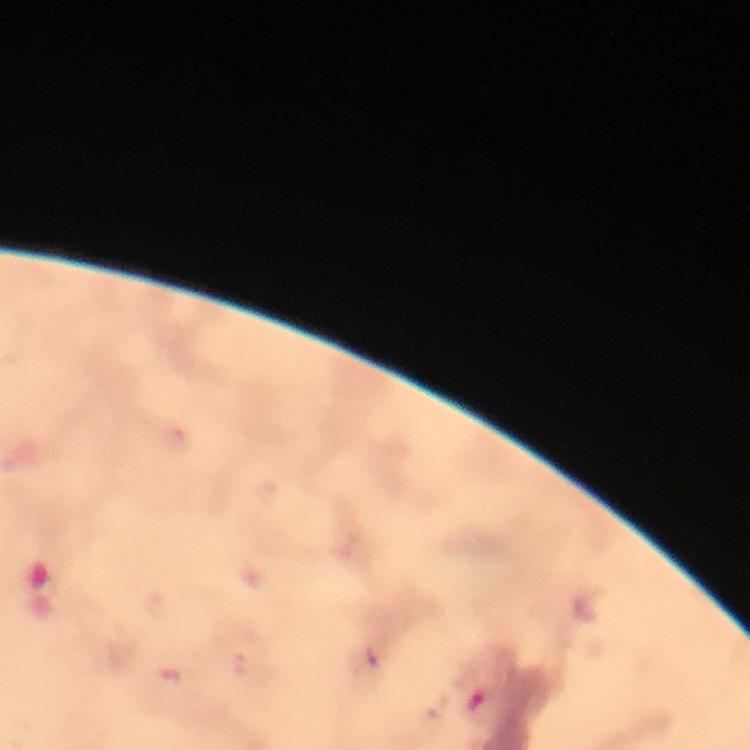
preparation = thick blood smear
stain = Giemsa
Plasmodium parasite locations = approximate centers as [x, y] in pixels: [376, 656], [476, 703]
magnification = 100x
immersion oil = applied
context = from a malaria diagnostic workup
capture = smartphone camera through the microscope
cropped from = one field of view
image size = 750×750 pixels